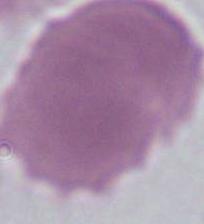
Micrograph. 1000x magnification. A red blood cell is seen.